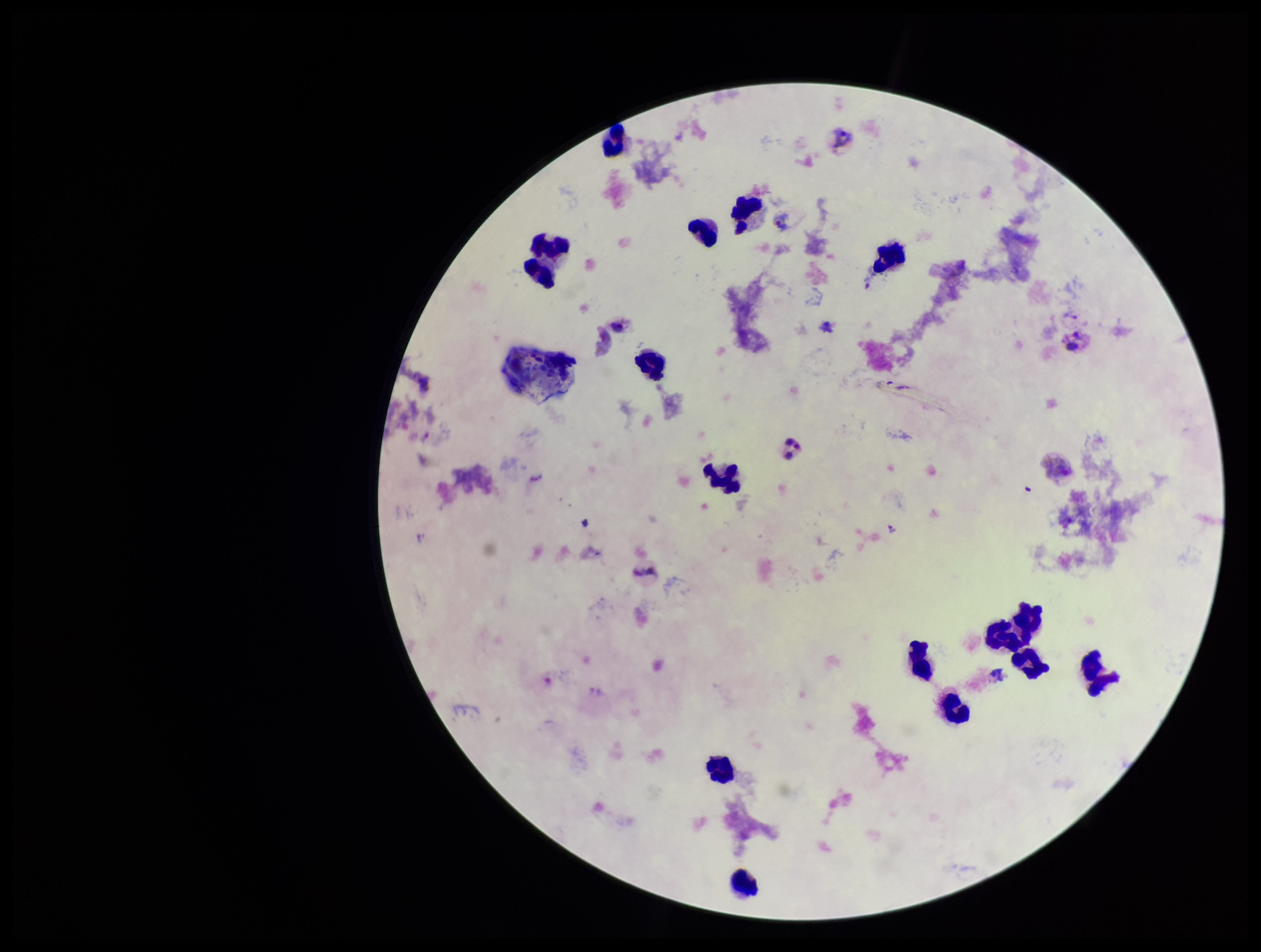
species_reported_for_this_patient: Plasmodium vivax
plasmodium_parasites: detected
image_size: 1261×952 pixels
field_of_view: single
stain: Giemsa
patient_malaria_status: positive
capture: smartphone photograph through the microscope eyepiece
parasite_count: 1
preparation: thick smear
leukocyte_count: 15